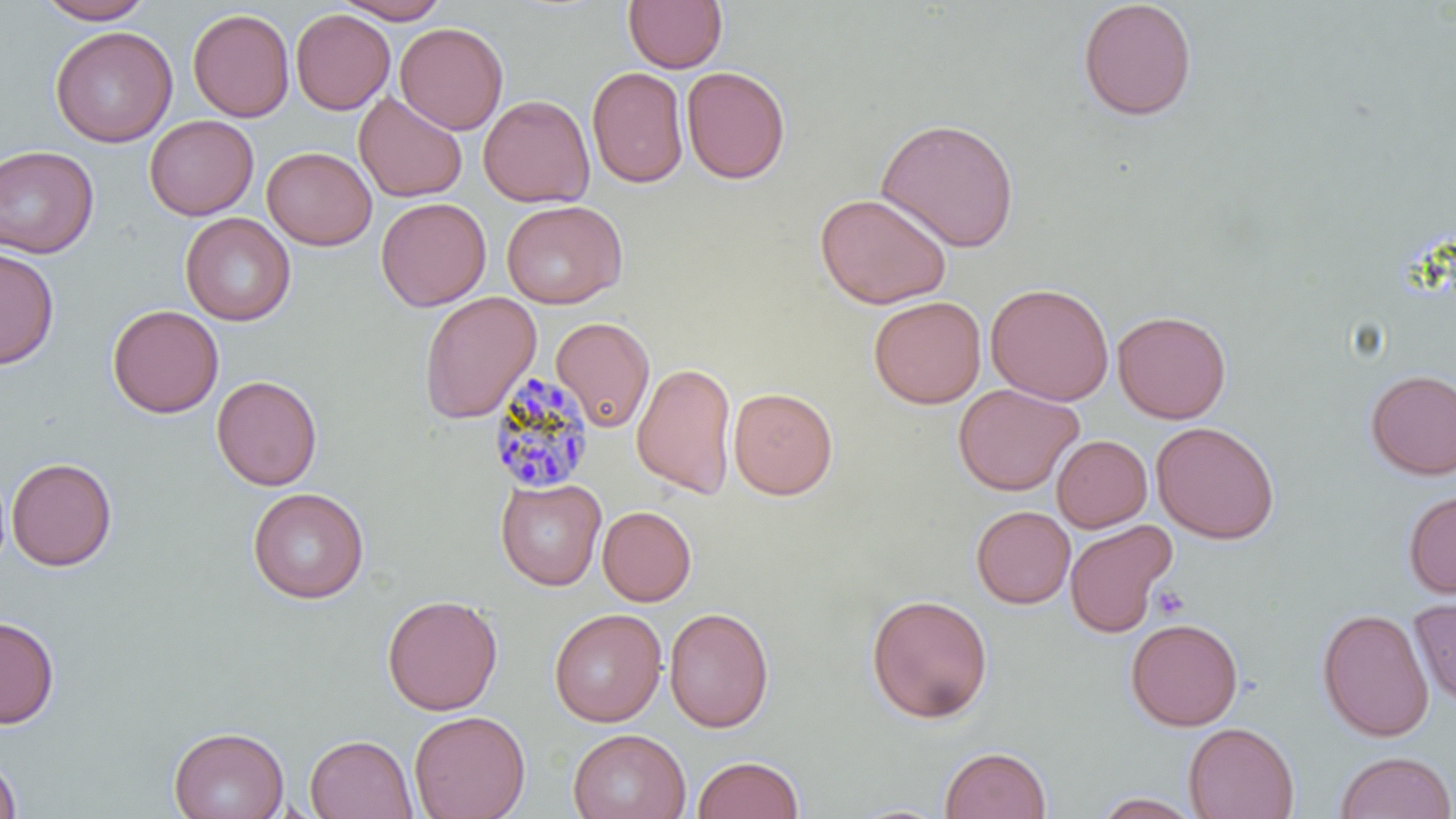 Approximate bounding boxes as named x1/y1/x2/y2 corners in pixels. Uninfected red blood cell locations: (x1=34, y1=0, x2=155, y2=24), (x1=333, y1=0, x2=451, y2=23), (x1=623, y1=0, x2=728, y2=73), (x1=1077, y1=0, x2=1198, y2=121), (x1=188, y1=8, x2=294, y2=122), (x1=290, y1=9, x2=395, y2=114), (x1=395, y1=22, x2=508, y2=135), (x1=50, y1=26, x2=177, y2=147), (x1=681, y1=65, x2=791, y2=184), (x1=586, y1=66, x2=689, y2=189), (x1=354, y1=92, x2=467, y2=202), (x1=478, y1=94, x2=594, y2=207), (x1=144, y1=115, x2=258, y2=220), (x1=875, y1=117, x2=1021, y2=253), (x1=0, y1=145, x2=99, y2=259), (x1=262, y1=146, x2=377, y2=250), (x1=815, y1=192, x2=953, y2=309), (x1=376, y1=197, x2=491, y2=311), (x1=501, y1=199, x2=627, y2=309), (x1=180, y1=212, x2=296, y2=326), (x1=0, y1=246, x2=60, y2=370), (x1=985, y1=282, x2=1115, y2=405), (x1=418, y1=291, x2=541, y2=424), (x1=868, y1=295, x2=987, y2=409), (x1=107, y1=304, x2=224, y2=418), (x1=1112, y1=310, x2=1231, y2=424), (x1=550, y1=317, x2=655, y2=433), (x1=632, y1=361, x2=738, y2=499), (x1=1364, y1=369, x2=1456, y2=480), (x1=211, y1=375, x2=323, y2=491), (x1=953, y1=383, x2=1083, y2=496), (x1=728, y1=387, x2=838, y2=500), (x1=1151, y1=421, x2=1280, y2=544), (x1=1051, y1=435, x2=1152, y2=532), (x1=6, y1=457, x2=118, y2=571), (x1=495, y1=478, x2=606, y2=591), (x1=247, y1=486, x2=369, y2=604), (x1=1402, y1=489, x2=1456, y2=599), (x1=597, y1=505, x2=697, y2=606), (x1=971, y1=505, x2=1075, y2=609), (x1=1064, y1=519, x2=1176, y2=638), (x1=865, y1=593, x2=994, y2=724), (x1=381, y1=594, x2=503, y2=715), (x1=1409, y1=597, x2=1456, y2=707), (x1=664, y1=606, x2=774, y2=732), (x1=1316, y1=607, x2=1434, y2=742), (x1=549, y1=608, x2=666, y2=726), (x1=0, y1=615, x2=59, y2=729), (x1=1125, y1=617, x2=1244, y2=731), (x1=409, y1=710, x2=530, y2=819), (x1=1183, y1=721, x2=1300, y2=819), (x1=168, y1=726, x2=289, y2=819), (x1=568, y1=728, x2=690, y2=819), (x1=305, y1=734, x2=417, y2=818), (x1=940, y1=746, x2=1052, y2=819), (x1=1333, y1=751, x2=1455, y2=819), (x1=0, y1=753, x2=22, y2=818), (x1=692, y1=755, x2=804, y2=819), (x1=1088, y1=791, x2=1206, y2=818). Platelet locations: (x1=1150, y1=585, x2=1190, y2=621). Plasmodium malariae-infected red blood cell locations: (x1=485, y1=371, x2=597, y2=496). Slide-level diagnosis: Plasmodium malariae. Image is 1456×819 pixels. Single field of view. Light microscopy. Captured at 1000x magnification. Thin blood film. May-Grünwald-Giemsa-stained preparation.